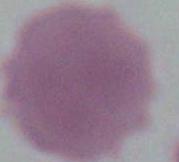
magnification: 1000x
modality: micrograph
identification: erythrocyte